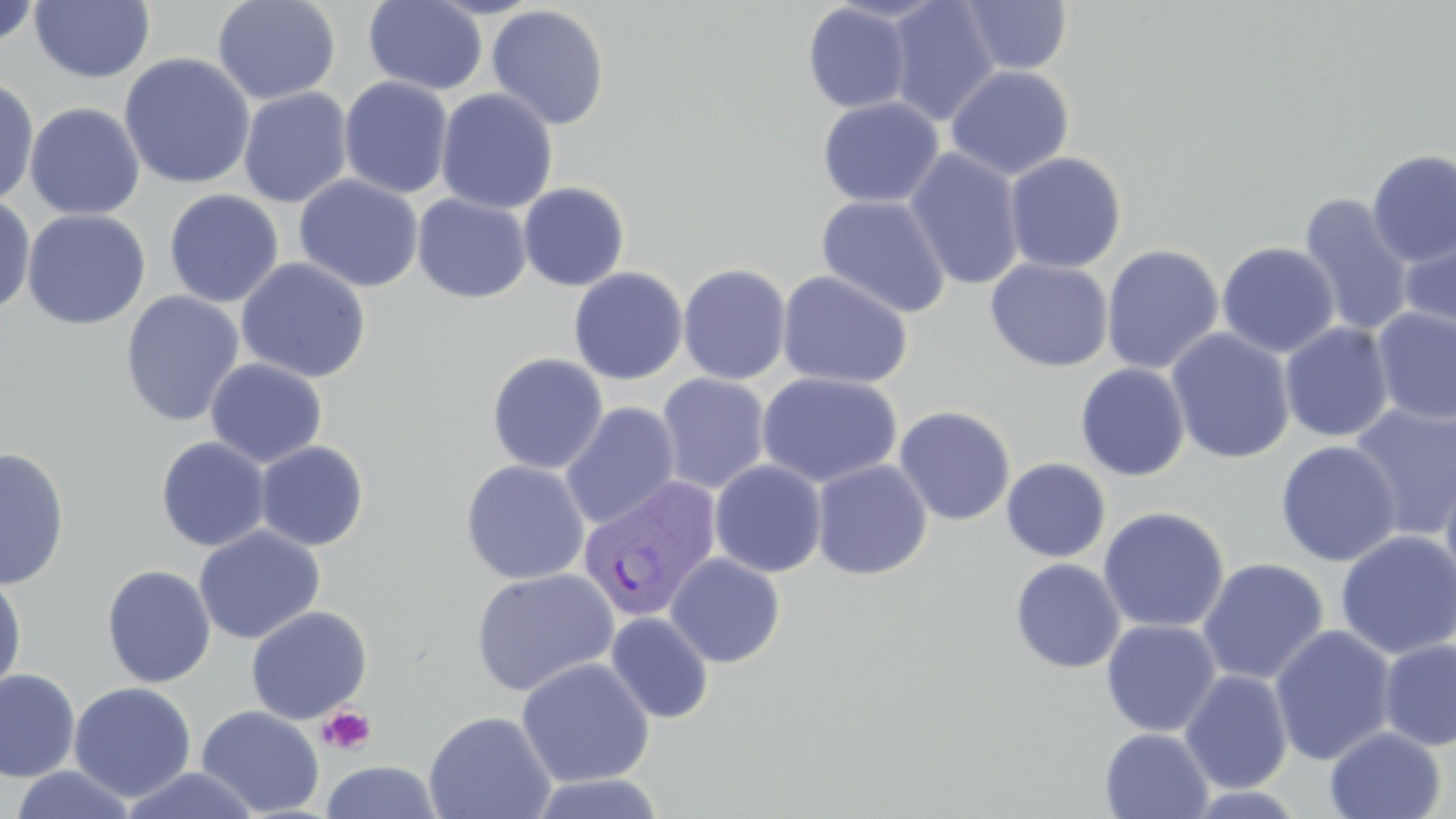

Summary:
  - Coordinate format: approximate bounding boxes as named x1/y1/x2/y2 corners in pixels
  - Plasmodium vivax-infected red blood cell locations: (x1=577, y1=476, x2=722, y2=624)
  - Platelet locations: (x1=317, y1=705, x2=377, y2=755)
  - Uninfected red blood cell locations: (x1=29, y1=0, x2=155, y2=83), (x1=212, y1=1, x2=341, y2=105), (x1=363, y1=1, x2=488, y2=95), (x1=883, y1=1, x2=1001, y2=126), (x1=956, y1=1, x2=1074, y2=75), (x1=0, y1=2, x2=42, y2=50), (x1=802, y1=2, x2=914, y2=114), (x1=486, y1=5, x2=611, y2=130), (x1=118, y1=52, x2=256, y2=190), (x1=946, y1=65, x2=1075, y2=181), (x1=0, y1=75, x2=40, y2=207), (x1=338, y1=76, x2=454, y2=199), (x1=238, y1=87, x2=353, y2=208), (x1=435, y1=88, x2=558, y2=214), (x1=817, y1=96, x2=943, y2=208), (x1=25, y1=102, x2=145, y2=220), (x1=904, y1=147, x2=1026, y2=291), (x1=1366, y1=150, x2=1456, y2=267), (x1=1004, y1=151, x2=1127, y2=274), (x1=294, y1=174, x2=424, y2=293), (x1=517, y1=182, x2=630, y2=291), (x1=164, y1=189, x2=284, y2=307), (x1=0, y1=193, x2=36, y2=316), (x1=412, y1=194, x2=532, y2=303), (x1=816, y1=194, x2=951, y2=319), (x1=1297, y1=194, x2=1415, y2=337), (x1=22, y1=208, x2=152, y2=330), (x1=1399, y1=219, x2=1456, y2=343), (x1=1216, y1=241, x2=1340, y2=358), (x1=1101, y1=244, x2=1224, y2=375), (x1=1085, y1=247, x2=1200, y2=481), (x1=235, y1=257, x2=372, y2=383), (x1=985, y1=258, x2=1114, y2=372), (x1=678, y1=263, x2=792, y2=385), (x1=568, y1=267, x2=688, y2=385), (x1=776, y1=270, x2=913, y2=390), (x1=120, y1=291, x2=245, y2=427), (x1=1371, y1=307, x2=1456, y2=425), (x1=1279, y1=322, x2=1395, y2=443), (x1=1166, y1=328, x2=1296, y2=465), (x1=486, y1=352, x2=608, y2=474), (x1=205, y1=358, x2=328, y2=468), (x1=1075, y1=362, x2=1191, y2=481), (x1=757, y1=371, x2=903, y2=488), (x1=655, y1=373, x2=771, y2=495), (x1=1348, y1=401, x2=1456, y2=541), (x1=560, y1=402, x2=681, y2=530), (x1=893, y1=405, x2=1016, y2=526), (x1=155, y1=436, x2=271, y2=552), (x1=1275, y1=440, x2=1402, y2=567), (x1=254, y1=441, x2=370, y2=551), (x1=0, y1=447, x2=71, y2=591), (x1=1002, y1=458, x2=1111, y2=562), (x1=460, y1=459, x2=590, y2=585), (x1=811, y1=459, x2=933, y2=580), (x1=709, y1=460, x2=827, y2=578), (x1=1440, y1=465, x2=1456, y2=598), (x1=1098, y1=506, x2=1230, y2=633), (x1=193, y1=525, x2=325, y2=645), (x1=1335, y1=530, x2=1456, y2=659), (x1=665, y1=552, x2=786, y2=668), (x1=1197, y1=557, x2=1329, y2=686), (x1=1010, y1=558, x2=1126, y2=674), (x1=102, y1=565, x2=216, y2=688), (x1=469, y1=568, x2=620, y2=697), (x1=0, y1=569, x2=28, y2=700), (x1=246, y1=605, x2=373, y2=724), (x1=605, y1=611, x2=714, y2=724), (x1=1101, y1=619, x2=1221, y2=737), (x1=1268, y1=625, x2=1397, y2=765), (x1=1378, y1=639, x2=1456, y2=751), (x1=515, y1=657, x2=655, y2=788), (x1=0, y1=669, x2=81, y2=782), (x1=1179, y1=669, x2=1294, y2=794), (x1=68, y1=682, x2=197, y2=802), (x1=196, y1=705, x2=325, y2=817), (x1=423, y1=710, x2=557, y2=819), (x1=1324, y1=726, x2=1446, y2=819), (x1=1099, y1=727, x2=1214, y2=819), (x1=320, y1=760, x2=444, y2=819), (x1=9, y1=765, x2=139, y2=818), (x1=117, y1=766, x2=263, y2=819), (x1=524, y1=772, x2=668, y2=818)
  - Slide-level diagnosis: Plasmodium vivax
  - Magnification: 1000x
  - Stain: May-Grünwald-Giemsa
  - Field of view: single
  - Preparation: thin blood smear
  - Modality: light microscopy
  - Image size: 1456×819 pixels